Mark where leukocytes are.
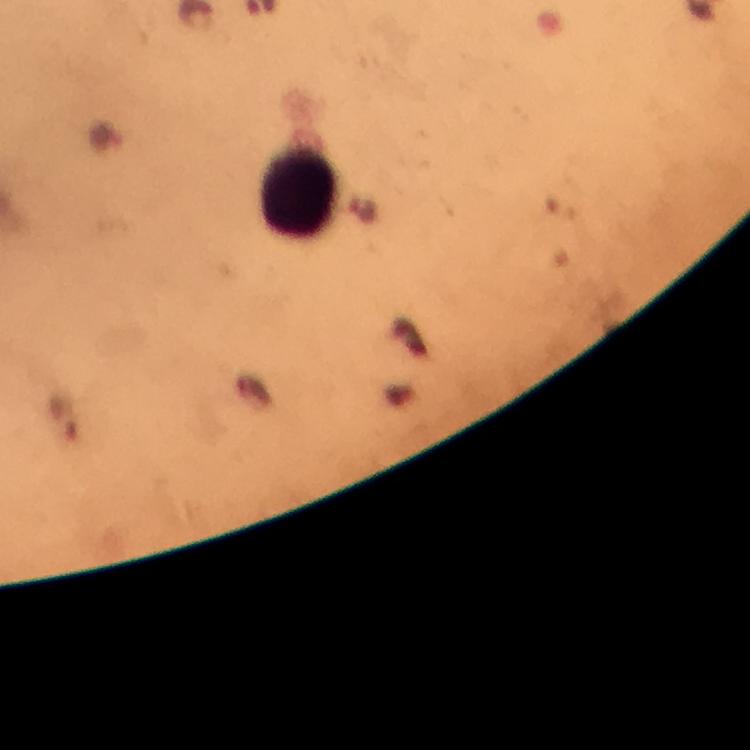
Approximate centers as [x, y] in pixels.
Leukocytes: [299, 193].

capture = smartphone mounted on the microscope
malaria parasites = none seen
immersion oil = used
cropped from = a single field of view
magnification = 100x
preparation = thick blood film
stain = Giemsa
context = from a malaria diagnostic workup
image size = 750×750 pixels